Classify this cell by malaria status.
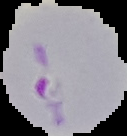
It is parasitized.

Summary:
  - Image type: segmented cell region with the area outside set to black
  - Image size: 127×136 pixels
  - Preparation: thin blood smear